Look for parasitized red blood cells.
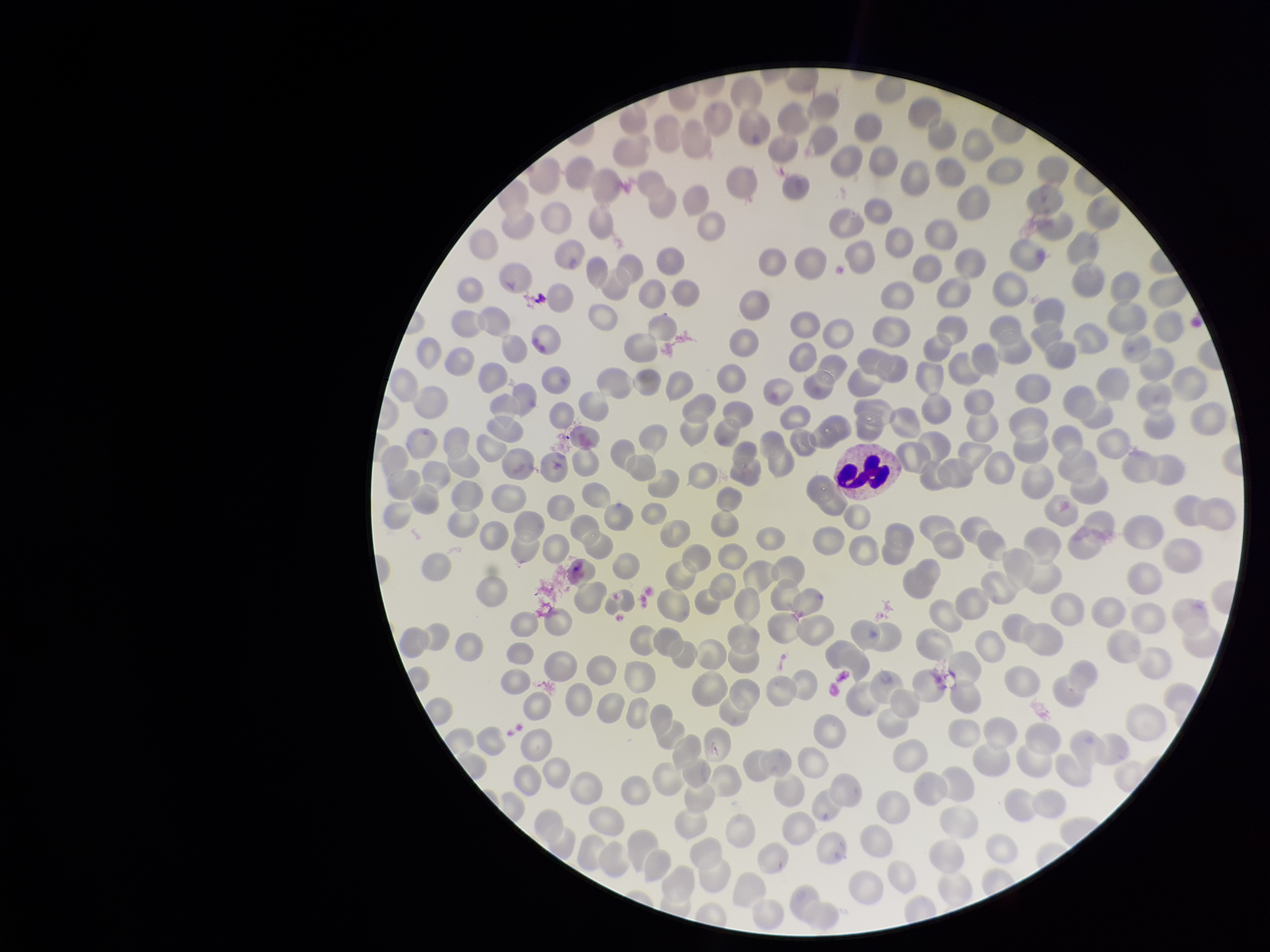
None identified.

parasitized red blood cell count = 0
capture = smartphone photograph through the microscope eyepiece
field of view = one from this slide
red blood cell count = 289
patient malaria status = negative
preparation = thin smear
image size = 1270×952 pixels
stain = Giemsa